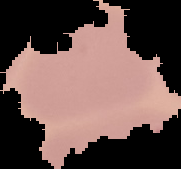

Summary:
  - Preparation: thin blood smear
  - Image type: cell region segmented out of the field of view; surrounding area masked to black
  - Result: negative for Plasmodium parasites
  - Image size: 181×169 pixels